Locate every Plasmodium malariae-infected red blood cell.
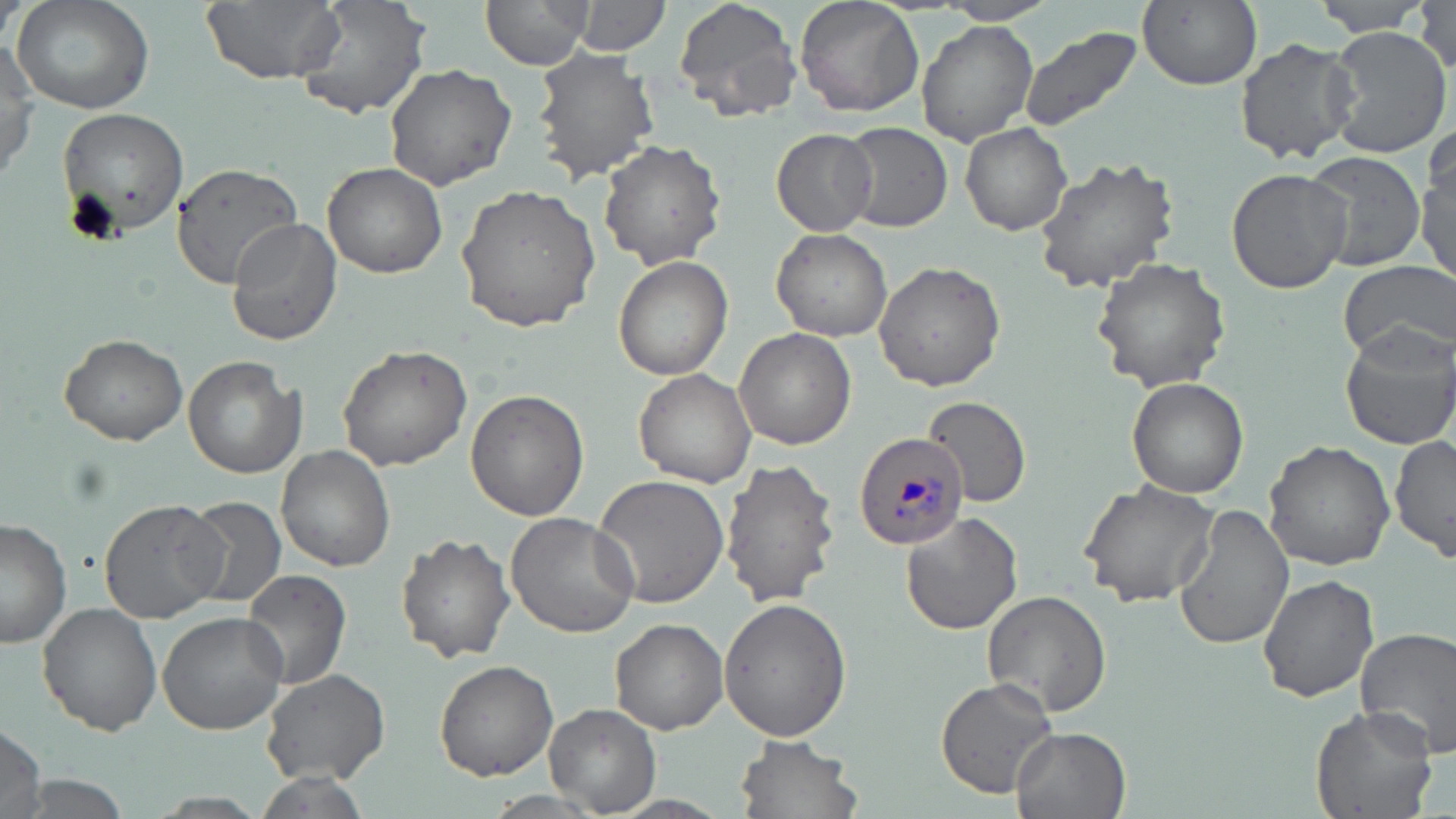

Approximate bounding boxes as named x1/y1/x2/y2 corners in pixels.
Plasmodium malariae-infected red blood cells: (x1=854, y1=430, x2=970, y2=550).

Uninfected red blood cell locations: (x1=9, y1=0, x2=155, y2=115), (x1=200, y1=0, x2=344, y2=85), (x1=291, y1=0, x2=432, y2=119), (x1=480, y1=0, x2=594, y2=70), (x1=571, y1=0, x2=671, y2=57), (x1=672, y1=0, x2=802, y2=121), (x1=795, y1=0, x2=925, y2=119), (x1=937, y1=0, x2=1057, y2=24), (x1=1138, y1=0, x2=1261, y2=92), (x1=1307, y1=1, x2=1436, y2=37), (x1=1412, y1=4, x2=1453, y2=71), (x1=917, y1=21, x2=1038, y2=146), (x1=1322, y1=26, x2=1453, y2=156), (x1=1018, y1=28, x2=1142, y2=135), (x1=1235, y1=37, x2=1359, y2=165), (x1=1, y1=41, x2=38, y2=187), (x1=531, y1=49, x2=660, y2=182), (x1=384, y1=65, x2=516, y2=188), (x1=54, y1=106, x2=189, y2=241), (x1=840, y1=122, x2=952, y2=232), (x1=961, y1=123, x2=1071, y2=236), (x1=771, y1=128, x2=879, y2=235), (x1=598, y1=138, x2=727, y2=270), (x1=1417, y1=143, x2=1455, y2=286), (x1=1302, y1=150, x2=1425, y2=273), (x1=1031, y1=156, x2=1181, y2=293), (x1=170, y1=161, x2=307, y2=288), (x1=322, y1=162, x2=448, y2=278), (x1=1225, y1=167, x2=1352, y2=295), (x1=453, y1=184, x2=603, y2=335), (x1=224, y1=219, x2=343, y2=347), (x1=772, y1=229, x2=891, y2=342), (x1=613, y1=255, x2=733, y2=380), (x1=1091, y1=257, x2=1231, y2=394), (x1=873, y1=260, x2=1005, y2=391), (x1=1338, y1=260, x2=1456, y2=364), (x1=1339, y1=323, x2=1456, y2=450), (x1=734, y1=326, x2=857, y2=450), (x1=58, y1=333, x2=190, y2=445), (x1=336, y1=345, x2=473, y2=471), (x1=184, y1=356, x2=306, y2=478), (x1=634, y1=370, x2=757, y2=487), (x1=1127, y1=378, x2=1250, y2=499), (x1=465, y1=390, x2=586, y2=521), (x1=921, y1=395, x2=1031, y2=508), (x1=1389, y1=434, x2=1455, y2=562), (x1=1263, y1=439, x2=1396, y2=573), (x1=276, y1=445, x2=396, y2=573), (x1=720, y1=459, x2=840, y2=611), (x1=593, y1=474, x2=733, y2=609), (x1=1078, y1=481, x2=1219, y2=610), (x1=181, y1=496, x2=287, y2=607), (x1=99, y1=497, x2=227, y2=624), (x1=1172, y1=503, x2=1295, y2=653), (x1=900, y1=510, x2=1024, y2=633), (x1=506, y1=513, x2=641, y2=639), (x1=0, y1=517, x2=74, y2=649), (x1=397, y1=535, x2=515, y2=664), (x1=241, y1=567, x2=351, y2=688), (x1=1256, y1=571, x2=1381, y2=704), (x1=982, y1=589, x2=1112, y2=719), (x1=718, y1=598, x2=852, y2=742), (x1=37, y1=603, x2=162, y2=735), (x1=157, y1=610, x2=289, y2=736), (x1=610, y1=617, x2=728, y2=734), (x1=1354, y1=626, x2=1456, y2=760), (x1=434, y1=659, x2=558, y2=780), (x1=259, y1=667, x2=390, y2=786), (x1=935, y1=677, x2=1060, y2=798), (x1=545, y1=703, x2=661, y2=813), (x1=1311, y1=705, x2=1437, y2=819), (x1=0, y1=722, x2=48, y2=819), (x1=1011, y1=727, x2=1131, y2=819), (x1=735, y1=734, x2=864, y2=819), (x1=249, y1=770, x2=375, y2=818). Slide-level diagnosis: Plasmodium malariae. Thin blood film. May-Grünwald-Giemsa-stained preparation. Single field of view. Image is 1456×819 pixels. Captured at 1000x magnification. Light microscopy.